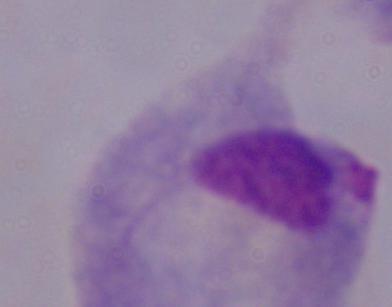
Summary:
  - Modality: micrograph
  - Magnification: 1000x
  - Identification: trichomonad